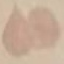
Summary:
  - Malaria status: uninfected
  - Capture: smartphone through the microscope eyepiece
  - Preparation: thin smear
  - Image type: automatically extracted cell patch, resized to 64 × 64 pixels
  - Stain: Giemsa